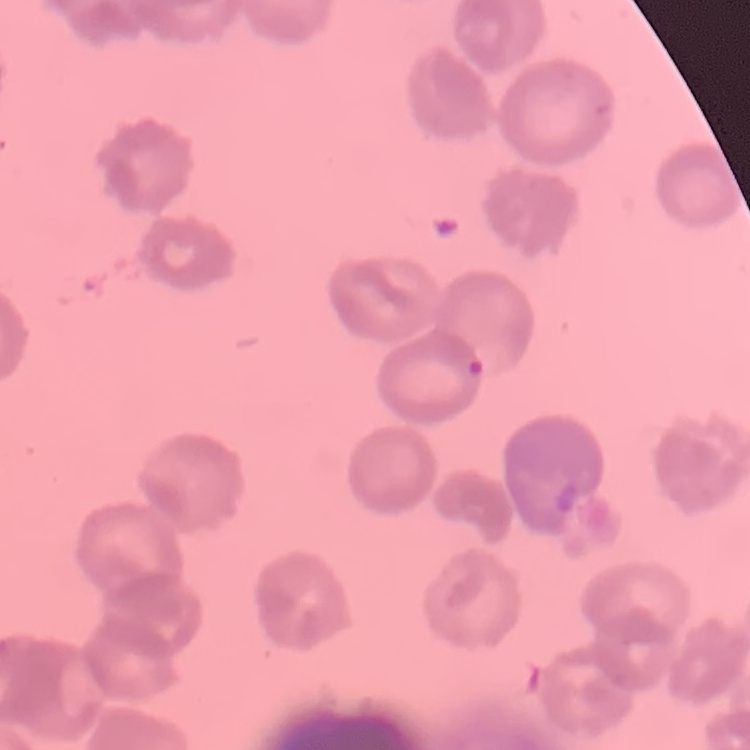

The erythrocytes exhibit rouleaux formation. Stained with either Field's or Giemsa. Thin blood smear. One tile cut from a larger photomicrograph.